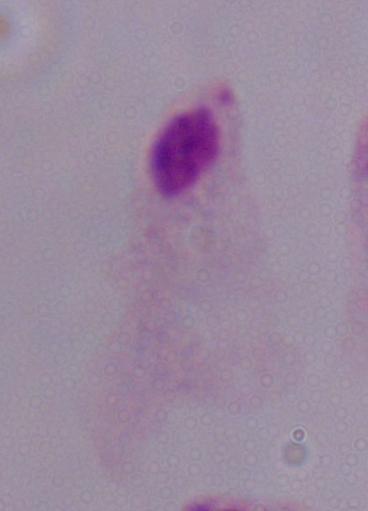
Captured at 1000x magnification. A trichomonad is shown. Micrograph.